State which cell type is depicted.
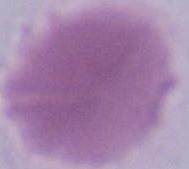
This is an erythrocyte.

Photomicrograph. Captured at 1000x magnification.